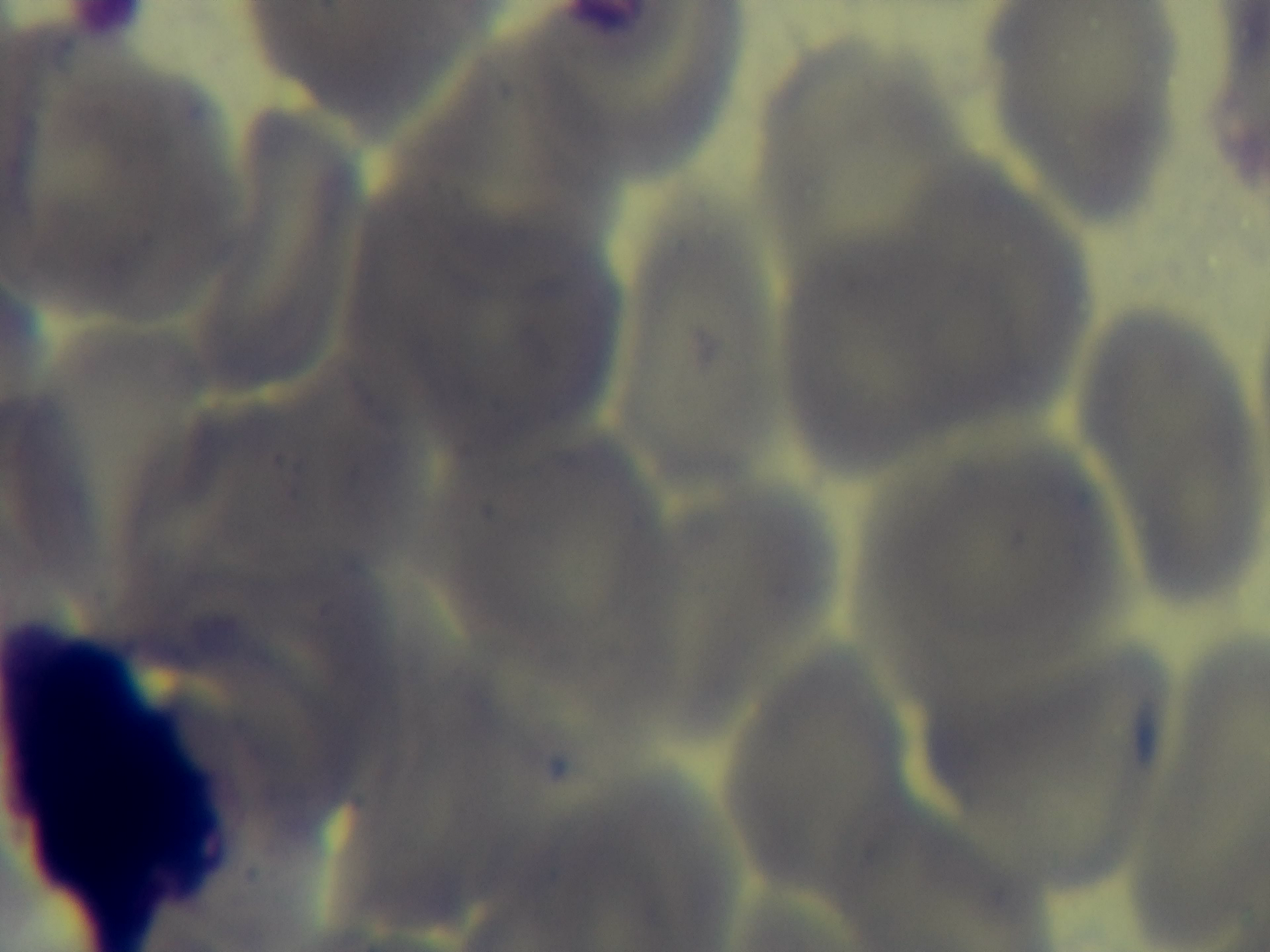 Preparation: thin. Malaria status: uninfected. Photomicrograph. Captured with a mounted 4K digital camera. One field from the slide. Giemsa-stained. Oil-immersion objective, 100x.